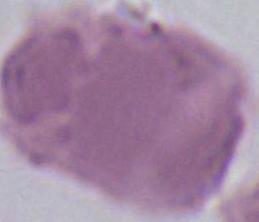
identification = erythrocyte
modality = photomicrograph
magnification = 1000x